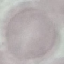
malaria status = uninfected
image type = cell patch, automatically extracted from a larger field of view and resized to 64 × 64 pixels
stain = Giemsa
preparation = thin blood smear
capture = smartphone through the microscope eyepiece